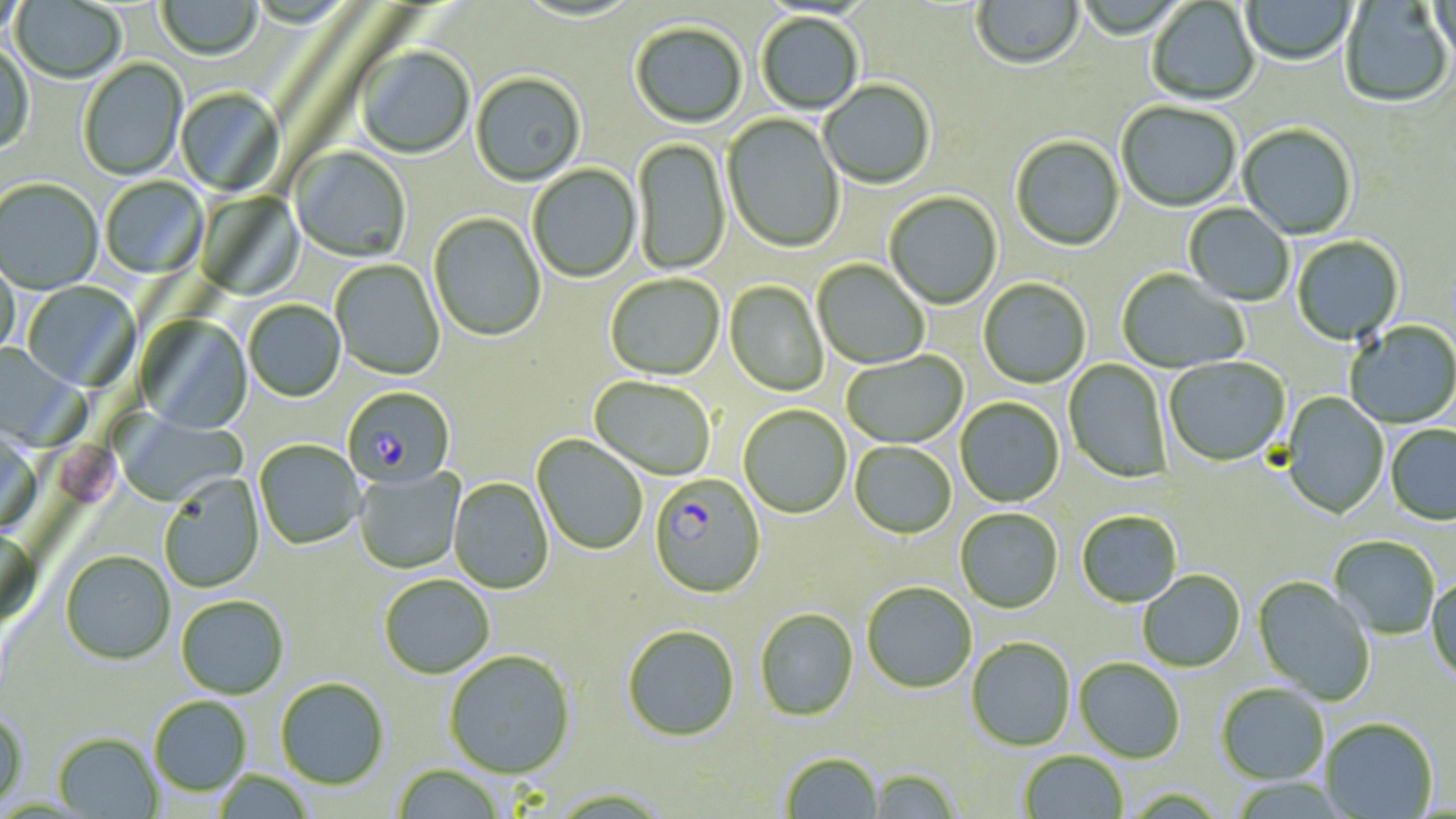

Summary:
  - Coordinate format: approximate bounding boxes as named x1/y1/x2/y2 corners in pixels
  - Uninfected red blood cell locations: (x1=157, y1=0, x2=263, y2=61), (x1=972, y1=0, x2=1084, y2=73), (x1=1242, y1=0, x2=1356, y2=67), (x1=1431, y1=0, x2=1456, y2=70), (x1=0, y1=1, x2=28, y2=39), (x1=11, y1=1, x2=126, y2=85), (x1=515, y1=1, x2=643, y2=24), (x1=1146, y1=1, x2=1260, y2=106), (x1=1339, y1=1, x2=1453, y2=110), (x1=756, y1=13, x2=864, y2=115), (x1=630, y1=23, x2=747, y2=129), (x1=0, y1=45, x2=34, y2=158), (x1=356, y1=47, x2=474, y2=160), (x1=78, y1=59, x2=188, y2=181), (x1=471, y1=74, x2=586, y2=188), (x1=820, y1=81, x2=935, y2=190), (x1=176, y1=88, x2=284, y2=196), (x1=1116, y1=103, x2=1241, y2=213), (x1=722, y1=113, x2=844, y2=254), (x1=1238, y1=125, x2=1357, y2=240), (x1=1010, y1=136, x2=1124, y2=253), (x1=632, y1=138, x2=731, y2=277), (x1=291, y1=147, x2=411, y2=263), (x1=528, y1=164, x2=641, y2=283), (x1=100, y1=177, x2=208, y2=279), (x1=0, y1=179, x2=102, y2=295), (x1=196, y1=191, x2=304, y2=301), (x1=884, y1=192, x2=1002, y2=310), (x1=1184, y1=203, x2=1293, y2=306), (x1=428, y1=213, x2=546, y2=342), (x1=1292, y1=236, x2=1404, y2=345), (x1=0, y1=257, x2=19, y2=362), (x1=330, y1=259, x2=444, y2=381), (x1=812, y1=260, x2=929, y2=370), (x1=1116, y1=270, x2=1248, y2=374), (x1=605, y1=275, x2=725, y2=381), (x1=978, y1=278, x2=1091, y2=389), (x1=725, y1=281, x2=829, y2=397), (x1=21, y1=282, x2=141, y2=392), (x1=243, y1=300, x2=345, y2=402), (x1=136, y1=315, x2=252, y2=435), (x1=1345, y1=321, x2=1456, y2=429), (x1=0, y1=342, x2=84, y2=451), (x1=841, y1=350, x2=968, y2=449), (x1=1164, y1=357, x2=1291, y2=468), (x1=1064, y1=359, x2=1172, y2=484), (x1=589, y1=376, x2=715, y2=481), (x1=1281, y1=392, x2=1389, y2=519), (x1=955, y1=398, x2=1064, y2=508), (x1=739, y1=405, x2=851, y2=518), (x1=112, y1=411, x2=247, y2=507), (x1=1385, y1=425, x2=1456, y2=525), (x1=0, y1=429, x2=42, y2=539), (x1=532, y1=435, x2=647, y2=555), (x1=255, y1=440, x2=365, y2=549), (x1=850, y1=442, x2=956, y2=539), (x1=353, y1=468, x2=465, y2=574), (x1=158, y1=476, x2=264, y2=593), (x1=449, y1=477, x2=553, y2=594), (x1=955, y1=509, x2=1063, y2=614), (x1=1077, y1=512, x2=1182, y2=608), (x1=0, y1=528, x2=41, y2=629), (x1=1329, y1=536, x2=1440, y2=640), (x1=60, y1=551, x2=175, y2=665), (x1=1138, y1=570, x2=1246, y2=672), (x1=379, y1=575, x2=494, y2=679), (x1=1252, y1=576, x2=1375, y2=706), (x1=1427, y1=576, x2=1456, y2=685), (x1=862, y1=582, x2=977, y2=693), (x1=176, y1=596, x2=288, y2=700), (x1=755, y1=608, x2=858, y2=721), (x1=622, y1=624, x2=740, y2=742), (x1=966, y1=637, x2=1076, y2=751), (x1=444, y1=651, x2=575, y2=779), (x1=1074, y1=658, x2=1185, y2=763), (x1=276, y1=678, x2=390, y2=791), (x1=1216, y1=684, x2=1329, y2=786), (x1=149, y1=696, x2=251, y2=797), (x1=0, y1=710, x2=28, y2=811), (x1=1321, y1=719, x2=1438, y2=818), (x1=53, y1=734, x2=162, y2=818), (x1=1019, y1=751, x2=1128, y2=818), (x1=781, y1=753, x2=884, y2=818), (x1=393, y1=765, x2=503, y2=819), (x1=867, y1=768, x2=962, y2=818), (x1=213, y1=770, x2=315, y2=818)
  - Platelet locations: (x1=58, y1=444, x2=121, y2=509)
  - Plasmodium falciparum-infected red blood cell locations: (x1=342, y1=386, x2=456, y2=490), (x1=648, y1=474, x2=766, y2=598)
  - Slide-level diagnosis: Plasmodium falciparum
  - Image size: 1456×819 pixels
  - Preparation: thin blood smear
  - Stain: May-Grünwald-Giemsa
  - Modality: light microscopy
  - Magnification: 1000x
  - Field of view: one of a larger specimen